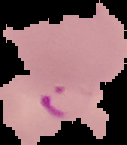 The area outside the segmented cell region is set to black. Result: malaria parasites identified. Image is 127×145 pixels. From a thin blood film.